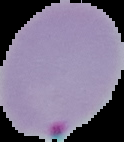
image_size: 124×142 pixels
preparation: thin blood film
image_type: segmented cell region with the area outside set to black
result: malaria parasites detected